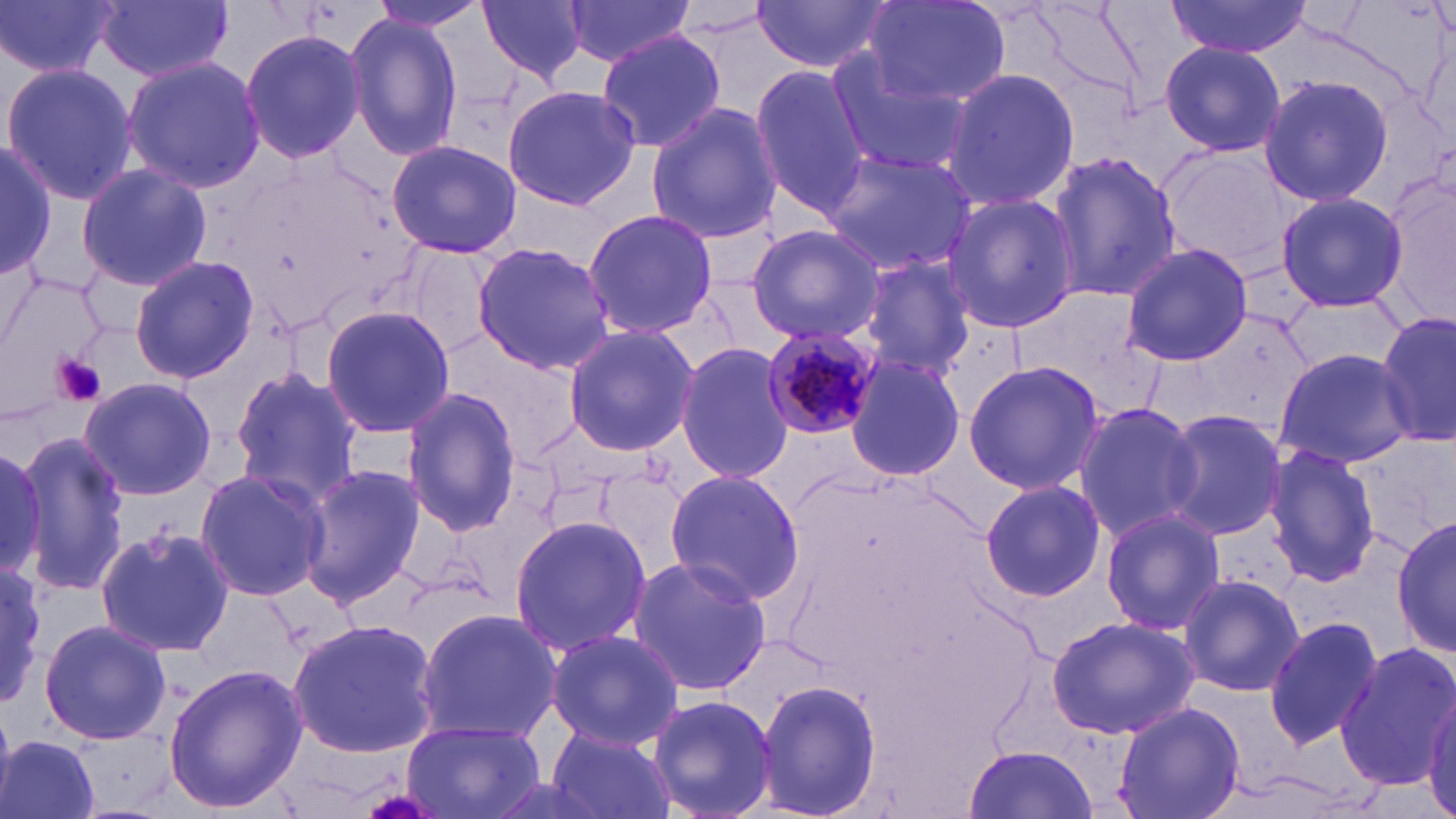

Approximate bounding boxes as (x1, y1, x2, y2) in pixels. Plasmodium malariae-infected red blood cell locations: (762, 325, 882, 446). Uninfected red blood cell locations: (0, 0, 118, 80), (96, 0, 233, 83), (363, 0, 489, 34), (477, 0, 590, 85), (563, 0, 699, 69), (862, 0, 1010, 105), (1023, 0, 1155, 117), (750, 1, 894, 73), (1167, 2, 1313, 58), (343, 11, 465, 161), (238, 26, 369, 165), (595, 31, 728, 154), (1160, 42, 1286, 157), (824, 49, 970, 177), (121, 55, 266, 192), (2, 61, 139, 206), (750, 65, 876, 218), (942, 67, 1080, 212), (1256, 75, 1395, 210), (501, 85, 641, 211), (645, 101, 782, 245), (0, 138, 57, 282), (386, 138, 522, 260), (1156, 146, 1300, 273), (1046, 148, 1181, 304), (819, 149, 978, 277), (1384, 159, 1456, 332), (74, 162, 213, 293), (1275, 190, 1409, 313), (942, 192, 1077, 334), (583, 208, 719, 338), (746, 225, 885, 344), (471, 241, 617, 375), (403, 242, 503, 358), (1121, 242, 1253, 367), (853, 254, 976, 380), (128, 255, 259, 384), (1284, 298, 1408, 369), (319, 305, 455, 437), (1376, 313, 1453, 446), (561, 323, 699, 456), (675, 342, 795, 482), (1272, 347, 1415, 466), (845, 353, 965, 484), (962, 360, 1103, 496), (227, 367, 365, 505), (79, 377, 219, 500), (402, 388, 521, 535), (1071, 402, 1206, 542), (1161, 409, 1287, 541), (15, 432, 133, 597), (0, 442, 51, 585), (1262, 445, 1383, 587), (297, 463, 426, 607), (193, 468, 330, 601), (663, 469, 806, 605), (979, 478, 1105, 601), (1100, 508, 1227, 636), (509, 515, 654, 654), (1393, 516, 1455, 656), (95, 524, 233, 658), (624, 555, 774, 696), (0, 565, 49, 705), (1177, 574, 1306, 697), (413, 606, 562, 743), (1045, 615, 1201, 740), (1263, 616, 1385, 752), (39, 617, 171, 746), (288, 619, 440, 758), (543, 627, 684, 750), (1337, 641, 1455, 793), (163, 662, 306, 815), (755, 676, 882, 819), (1423, 686, 1456, 819), (647, 694, 778, 819), (1111, 702, 1245, 819), (403, 717, 547, 819), (546, 723, 678, 819), (0, 734, 102, 819), (963, 744, 1099, 818). Platelet locations: (53, 355, 107, 407). Slide-level diagnosis: Plasmodium malariae. Thin blood film. Image is 1456×819 pixels. May-Grünwald-Giemsa-stained preparation. Captured at 1000x magnification. One field of a larger specimen. Optical microscopy.